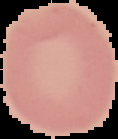
Malaria status: uninfected. Cell region segmented out of the field of view; the surrounding area is masked to black. From a thin blood smear. Image is 118×139 pixels.